Report the malaria status of this cell.
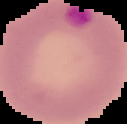
Parasitized.

Image is 127×124 pixels. Segmented cell region on a black background. From a thin blood film.